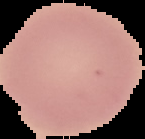

image size = 145×139 pixels
malaria status = uninfected
preparation = thin blood smear
image type = segmented cell region with the area outside set to black